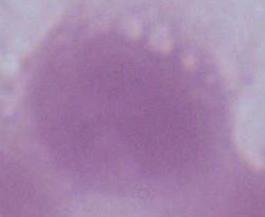

Summary:
  - Magnification: 1000x
  - Identification: red blood cell
  - Modality: photomicrograph